Classify this cell by malaria status.
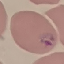
It is parasitized.

Summary:
  - Preparation: thin blood film
  - Capture: smartphone through the microscope eyepiece
  - Image type: automatically extracted cell patch, resized to 64 × 64 pixels
  - Stain: Giemsa